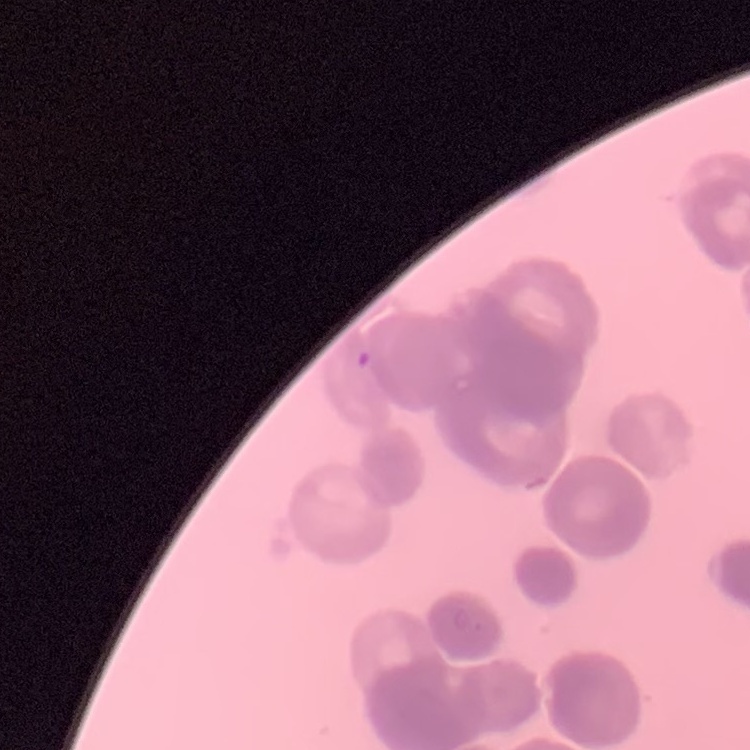

Summary:
  - Red blood cell morphology: rouleaux formation
  - Stain: Field's or Giemsa
  - Image type: one tile cut from a larger photomicrograph
  - Preparation: thin blood smear